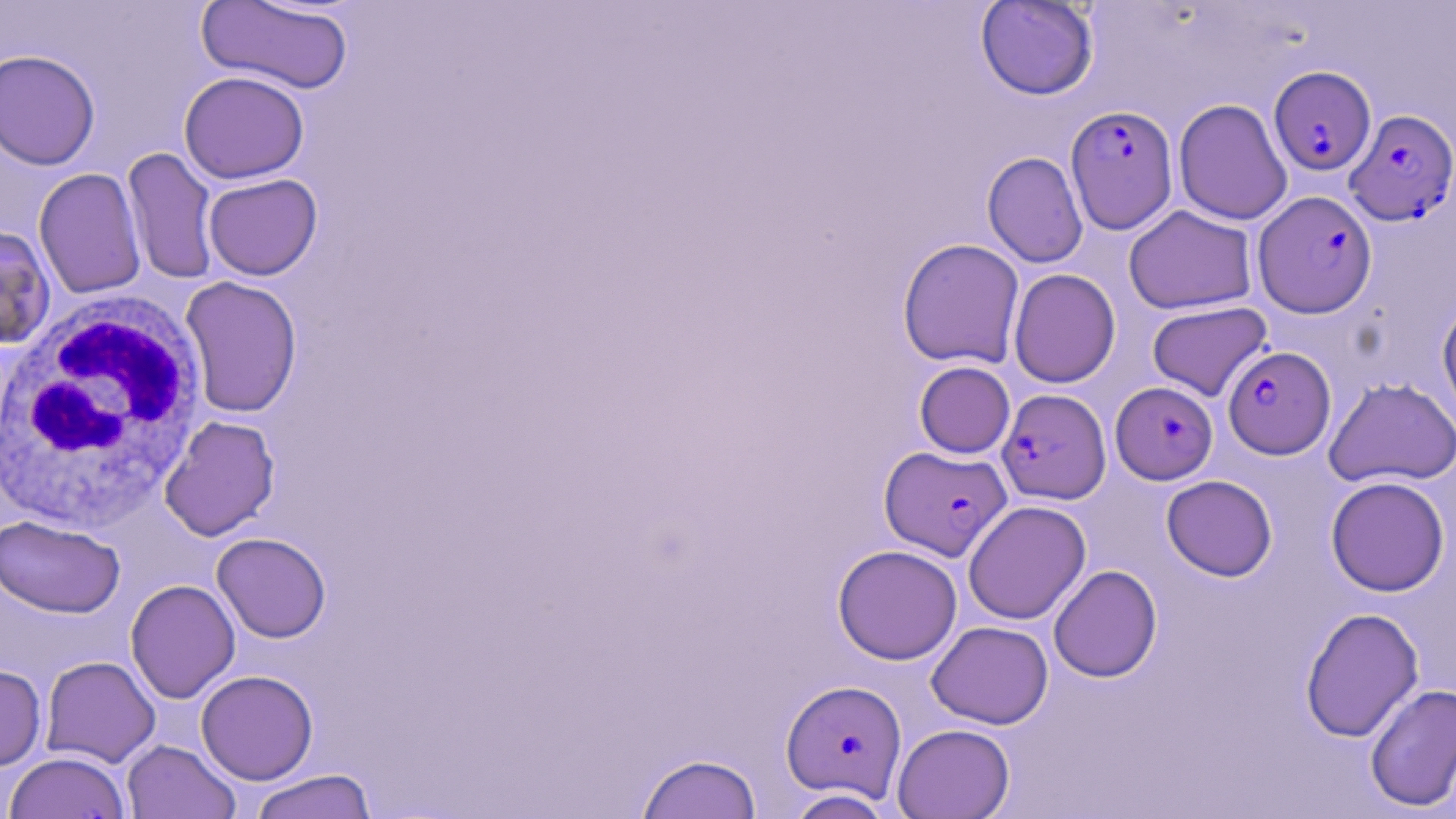

slide-level diagnosis = Plasmodium falciparum
image size = 1456×819 pixels
stain = May-Grünwald-Giemsa
uninfected red blood cell locations = approximate bounding boxes as named x1/y1/x2/y2 corners in pixels: (x1=197, y1=0, x2=354, y2=96), (x1=975, y1=1, x2=1099, y2=100), (x1=1, y1=48, x2=101, y2=171), (x1=178, y1=70, x2=310, y2=184), (x1=1173, y1=98, x2=1292, y2=225), (x1=122, y1=146, x2=220, y2=285), (x1=982, y1=151, x2=1088, y2=268), (x1=33, y1=167, x2=147, y2=299), (x1=203, y1=173, x2=322, y2=280), (x1=1123, y1=205, x2=1257, y2=314), (x1=0, y1=225, x2=55, y2=349), (x1=897, y1=238, x2=1024, y2=369), (x1=1008, y1=268, x2=1121, y2=388), (x1=180, y1=275, x2=303, y2=418), (x1=1437, y1=297, x2=1456, y2=426), (x1=1147, y1=301, x2=1273, y2=402), (x1=914, y1=361, x2=1015, y2=459), (x1=1324, y1=377, x2=1456, y2=488), (x1=159, y1=415, x2=280, y2=541), (x1=1161, y1=475, x2=1277, y2=580), (x1=1325, y1=476, x2=1450, y2=596), (x1=963, y1=500, x2=1091, y2=625), (x1=0, y1=515, x2=125, y2=618), (x1=211, y1=532, x2=331, y2=643), (x1=833, y1=544, x2=962, y2=665), (x1=1048, y1=565, x2=1162, y2=682), (x1=125, y1=579, x2=240, y2=704), (x1=1300, y1=607, x2=1424, y2=743), (x1=926, y1=621, x2=1053, y2=729), (x1=40, y1=656, x2=161, y2=768), (x1=0, y1=664, x2=47, y2=771), (x1=195, y1=669, x2=319, y2=785), (x1=1364, y1=683, x2=1456, y2=812), (x1=892, y1=723, x2=1015, y2=819), (x1=122, y1=739, x2=241, y2=819), (x1=4, y1=752, x2=130, y2=819), (x1=636, y1=752, x2=762, y2=819), (x1=247, y1=769, x2=378, y2=819), (x1=784, y1=789, x2=894, y2=818)
preparation = thin blood film
modality = optical microscopy
field of view = single
white blood cell locations = approximate bounding boxes as named x1/y1/x2/y2 corners in pixels: (x1=0, y1=290, x2=210, y2=533)
Plasmodium falciparum-infected red blood cell locations = approximate bounding boxes as named x1/y1/x2/y2 corners in pixels: (x1=1269, y1=66, x2=1376, y2=176), (x1=1065, y1=105, x2=1178, y2=233), (x1=1344, y1=108, x2=1456, y2=225), (x1=1253, y1=190, x2=1377, y2=318), (x1=1223, y1=345, x2=1335, y2=459), (x1=1111, y1=381, x2=1217, y2=484), (x1=997, y1=388, x2=1111, y2=505), (x1=879, y1=445, x2=1011, y2=561), (x1=781, y1=679, x2=907, y2=801)
magnification = 1000x